Identify the parasite.
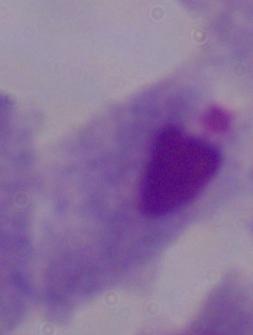

A trichomonad.

Summary:
  - Magnification: 1000x
  - Modality: photomicrograph